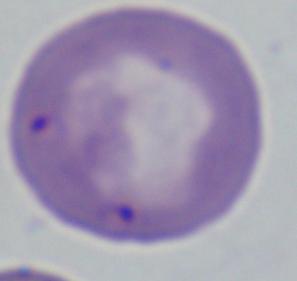
Photomicrograph. Captured at 1000x magnification. A Babesia parasite is seen.